Outline each blood parasite and name the species.
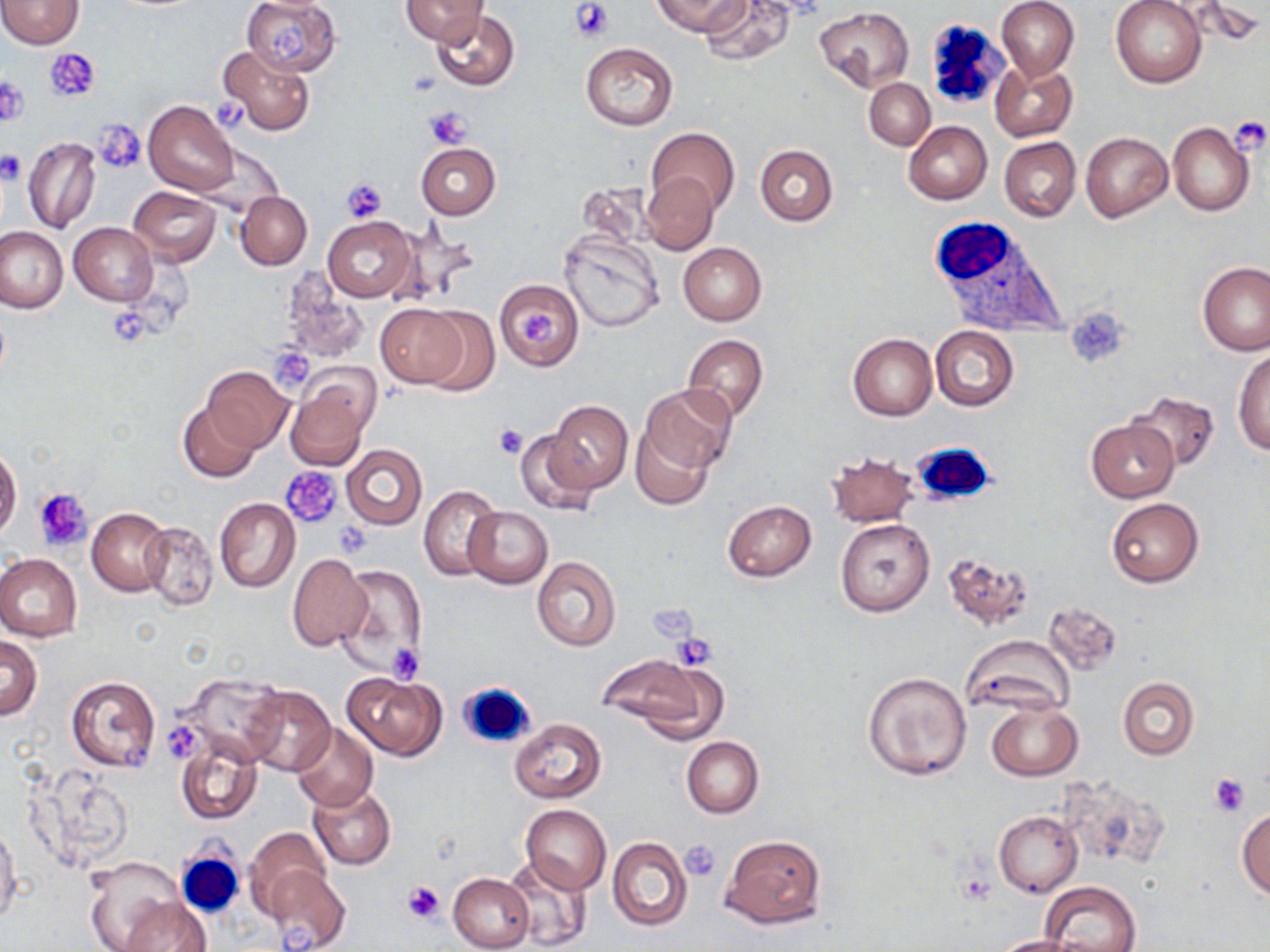
No blood parasites seen.

slide-level diagnosis = negative for blood parasites
magnification = 1000x
preparation = thin blood film
stain = May-Grünwald-Giemsa
uninfected red blood cell locations = approximate bounding boxes as (x1,y1)-(x2,y2) corner pairs in pixels: (0,0)-(84,49), (242,0)-(342,76), (402,0)-(487,46), (652,0)-(748,37), (698,0)-(794,67), (995,0)-(1079,80), (1111,0)-(1207,87), (815,8)-(915,92), (430,11)-(519,91), (579,42)-(679,130), (218,46)-(315,136), (990,60)-(1078,142), (864,78)-(935,149), (144,100)-(239,195), (903,121)-(992,205), (1167,122)-(1254,217), (646,127)-(741,216), (1081,132)-(1172,222), (999,136)-(1081,223), (23,137)-(100,234), (415,143)-(499,219), (756,144)-(839,226), (640,172)-(719,255), (575,181)-(657,249), (128,186)-(221,265), (235,191)-(312,270), (322,216)-(417,303), (393,221)-(480,310), (69,222)-(158,306), (0,227)-(66,313), (559,233)-(664,331), (678,241)-(766,325), (1198,262)-(1269,357), (280,277)-(369,366), (496,280)-(583,371), (374,303)-(469,387), (415,307)-(501,394), (931,326)-(1018,411), (848,333)-(937,420), (683,335)-(768,421), (1232,347)-(1270,454), (202,366)-(294,452), (285,376)-(374,471), (643,384)-(737,476), (1127,391)-(1220,472), (550,400)-(632,492), (178,401)-(259,483), (1084,419)-(1178,502), (633,425)-(716,510), (515,428)-(601,517), (341,443)-(427,530), (0,446)-(22,540), (827,451)-(919,528), (420,485)-(505,581), (214,496)-(300,592), (1107,497)-(1204,587), (723,500)-(817,580), (463,506)-(553,589), (88,508)-(171,595), (836,518)-(935,617), (141,521)-(219,612), (942,551)-(1033,631), (0,553)-(82,642), (287,554)-(369,651), (532,557)-(621,653), (332,562)-(428,682), (1044,602)-(1123,676), (962,632)-(1075,716), (0,635)-(42,720), (599,653)-(724,741), (861,670)-(972,783), (342,671)-(444,760), (174,672)-(286,767), (66,675)-(162,773), (1116,677)-(1199,760), (242,686)-(333,775), (986,700)-(1082,781), (510,719)-(605,802), (292,723)-(377,811), (682,736)-(764,818), (175,738)-(263,826), (29,765)-(136,872), (1058,773)-(1170,872), (308,785)-(396,870), (520,804)-(612,893), (993,811)-(1081,896), (1237,811)-(1270,900), (0,823)-(21,927), (244,827)-(335,922), (720,834)-(825,930), (607,837)-(692,930), (503,854)-(592,951), (82,855)-(185,952), (264,864)-(352,952), (448,873)-(534,952), (1041,882)-(1141,952), (119,896)-(212,952), (990,935)-(1082,952)
image size = 1270×952 pixels
white blood cell locations = approximate bounding boxes as (x1,y1)-(x2,y2) corner pairs in pixels: (927,16)-(1008,104), (928,215)-(1070,340), (911,441)-(996,506), (456,678)-(539,751), (176,849)-(245,917)
platelet locations = approximate bounding boxes as (x1,y1)-(x2,y2) corner pairs in pixels: (570,0)-(615,41), (271,26)-(310,65), (46,48)-(100,100), (1,78)-(28,128), (211,96)-(252,129), (426,106)-(473,149), (1230,117)-(1268,153), (95,121)-(147,173), (0,150)-(24,183), (340,179)-(387,224), (1066,308)-(1130,368), (109,309)-(148,345), (522,311)-(558,346), (269,349)-(312,389), (494,423)-(527,459), (282,468)-(344,528), (34,488)-(93,551), (669,635)-(716,671), (387,643)-(426,682), (166,725)-(202,764), (124,743)-(152,773), (1209,774)-(1249,816), (680,839)-(722,881), (401,878)-(447,923)
modality = light microscopy
field of view = single